Locate every malaria parasite.
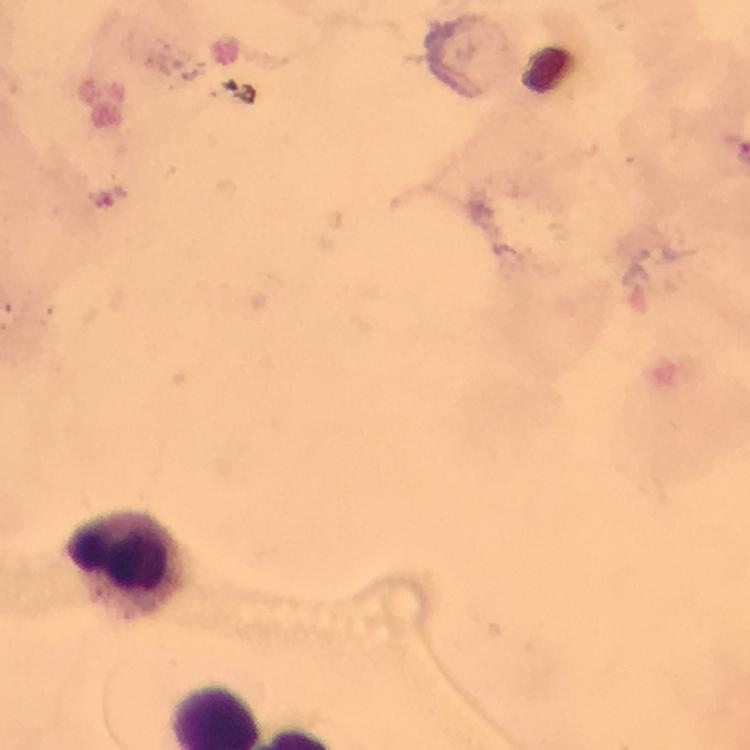
No malaria parasites seen.

magnification = 100x
context = from a malaria diagnostic workup
image size = 750×750 pixels
capture = smartphone camera through the microscope
immersion oil = applied
cropped from = one field of view
leukocyte locations = approximate centers as {x, y} in pixels: {126, 565}
stain = Giemsa
preparation = thick smear